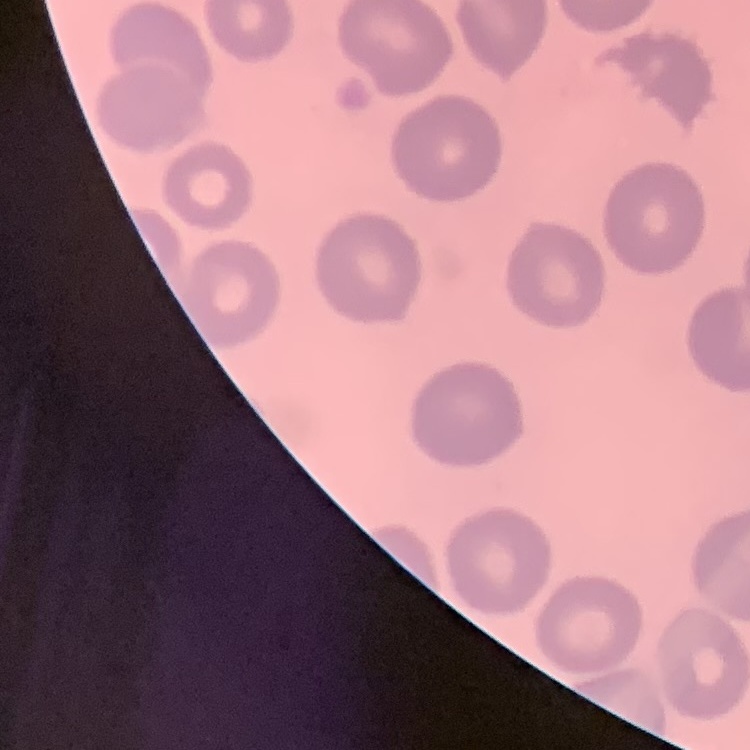

Summary:
  - Erythrocyte morphology: no rouleaux formation
  - Stain: Field's or Giemsa
  - Preparation: thin blood smear
  - Image type: one tile cut from a larger photomicrograph